Assess this cell for malaria.
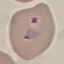
It is parasitized.

image_type: automatically extracted cell patch, resized to 64 × 64 pixels
stain: Giemsa
capture: smartphone camera at the microscope eyepiece
preparation: thin blood smear